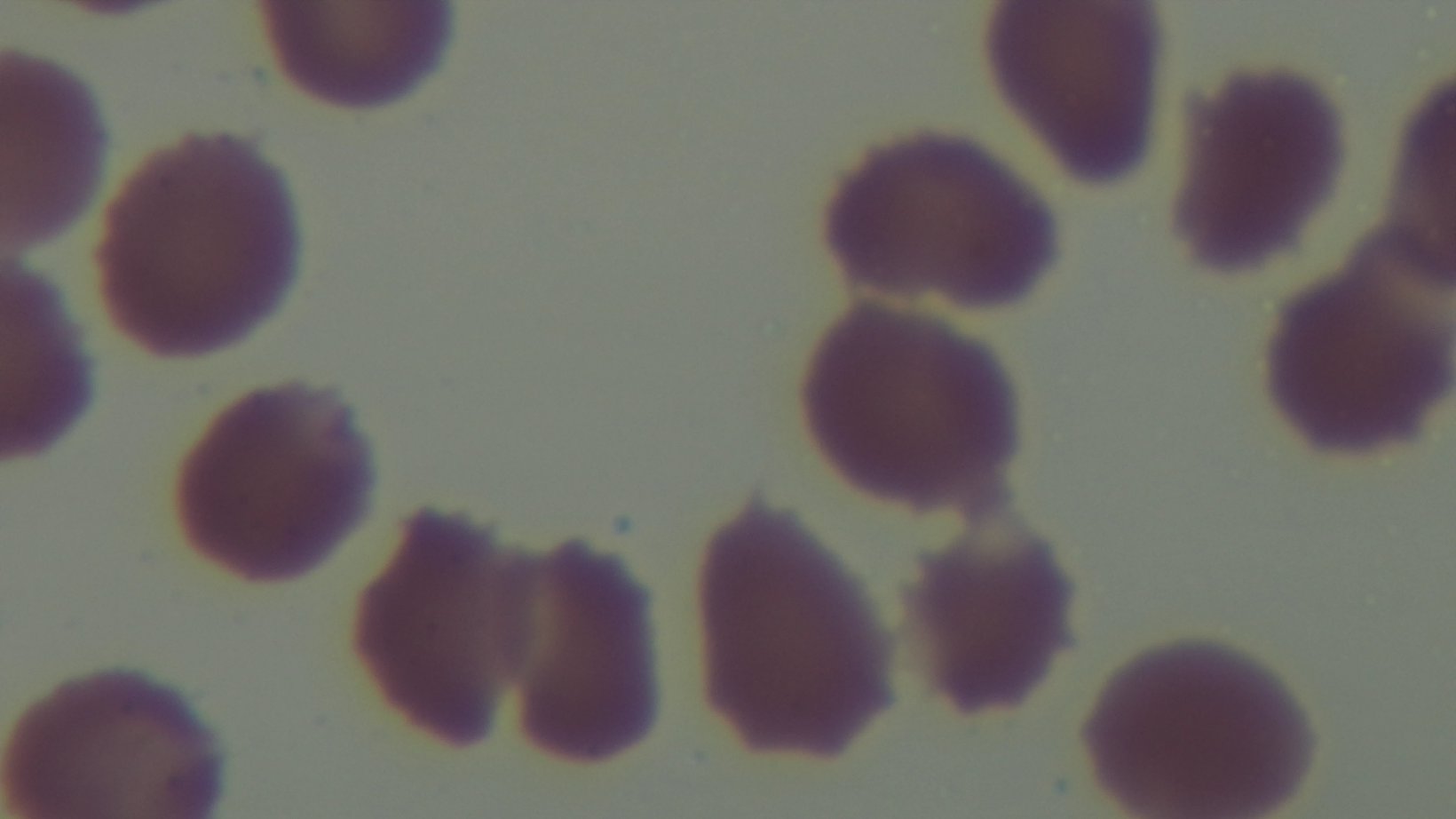

capture: mounted 4K digital camera
preparation: thin
stain: Giemsa
objective: 100x oil immersion
modality: light microscopy
malaria_status: negative
field_of_view: one from the slide